Locate and identify every blood parasite.
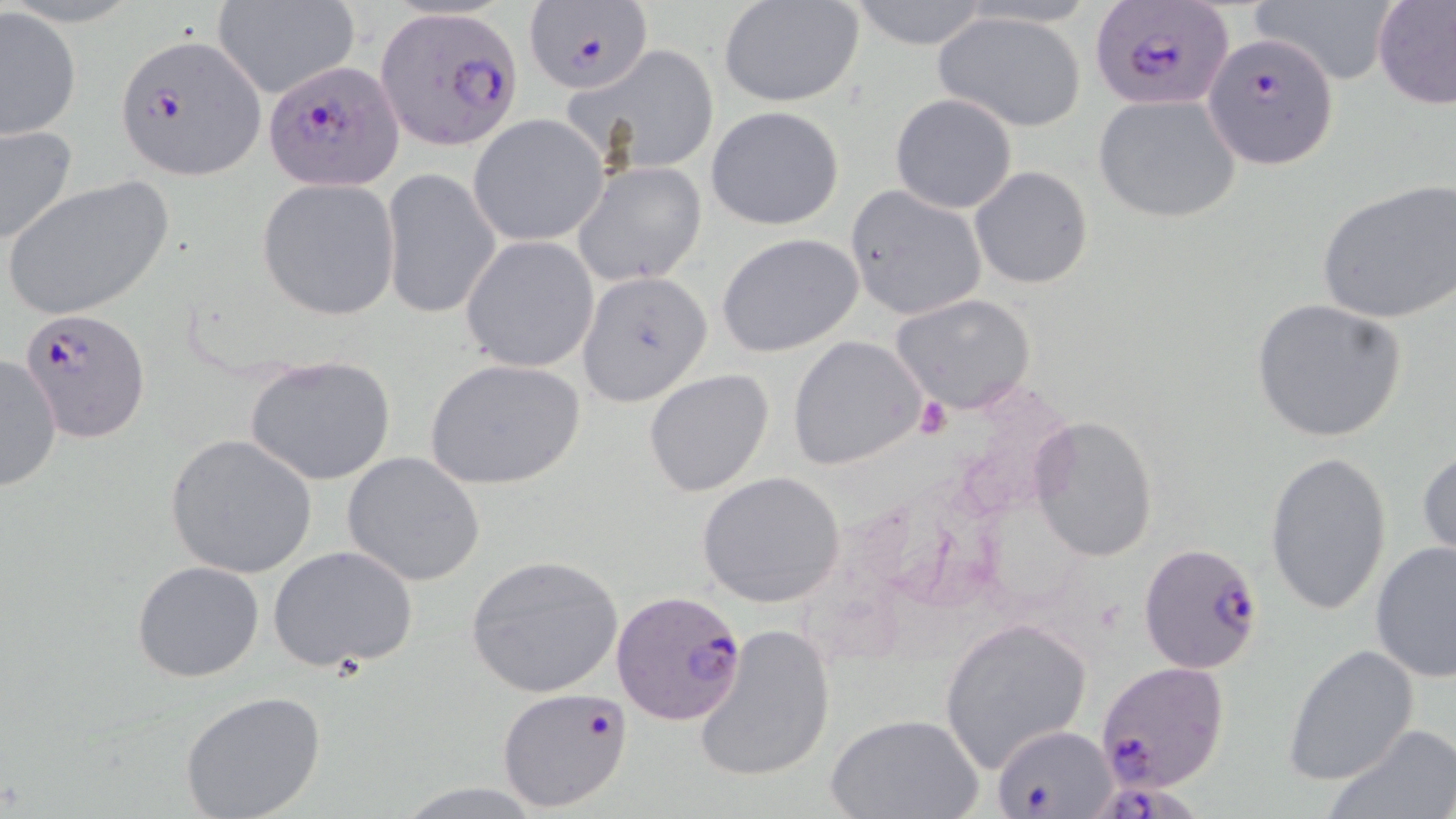
Approximate bounding boxes as named x1/y1/x2/y2 corners in pixels.
Plasmodium falciparum-infected red blood cells: (x1=1090, y1=0, x2=1235, y2=110), (x1=524, y1=4, x2=652, y2=97), (x1=375, y1=7, x2=523, y2=150), (x1=115, y1=32, x2=266, y2=178), (x1=1202, y1=33, x2=1338, y2=171), (x1=263, y1=62, x2=404, y2=192), (x1=19, y1=307, x2=149, y2=440), (x1=1139, y1=540, x2=1266, y2=676), (x1=611, y1=589, x2=749, y2=726), (x1=1096, y1=660, x2=1229, y2=794), (x1=498, y1=688, x2=633, y2=811), (x1=993, y1=725, x2=1115, y2=816), (x1=1094, y1=778, x2=1216, y2=819).
No Plasmodium ovale, Plasmodium malariae, Plasmodium vivax, Babesia divergens, or Trypanosoma brucei observed.

Summary:
  - Platelet locations: (x1=916, y1=396, x2=951, y2=440)
  - Uninfected red blood cell locations: (x1=718, y1=0, x2=864, y2=106), (x1=840, y1=0, x2=999, y2=49), (x1=1247, y1=0, x2=1401, y2=87), (x1=1373, y1=0, x2=1456, y2=109), (x1=212, y1=1, x2=358, y2=102), (x1=0, y1=3, x2=81, y2=141), (x1=933, y1=9, x2=1088, y2=132), (x1=573, y1=46, x2=723, y2=175), (x1=890, y1=93, x2=1018, y2=213), (x1=1095, y1=94, x2=1242, y2=224), (x1=705, y1=105, x2=844, y2=231), (x1=468, y1=114, x2=608, y2=246), (x1=0, y1=123, x2=78, y2=248), (x1=575, y1=162, x2=707, y2=285), (x1=969, y1=166, x2=1092, y2=288), (x1=381, y1=168, x2=501, y2=321), (x1=2, y1=174, x2=174, y2=321), (x1=257, y1=179, x2=401, y2=320), (x1=1317, y1=182, x2=1456, y2=323), (x1=845, y1=184, x2=987, y2=319), (x1=716, y1=233, x2=865, y2=358), (x1=461, y1=236, x2=599, y2=372), (x1=580, y1=268, x2=714, y2=417), (x1=891, y1=294, x2=1034, y2=413), (x1=1248, y1=297, x2=1408, y2=444), (x1=788, y1=335, x2=927, y2=471), (x1=0, y1=353, x2=63, y2=493), (x1=245, y1=355, x2=396, y2=486), (x1=424, y1=359, x2=586, y2=490), (x1=644, y1=369, x2=775, y2=499), (x1=1030, y1=417, x2=1158, y2=561), (x1=166, y1=434, x2=318, y2=579), (x1=1417, y1=447, x2=1456, y2=560), (x1=1264, y1=450, x2=1393, y2=617), (x1=342, y1=452, x2=486, y2=586), (x1=696, y1=471, x2=847, y2=607), (x1=1370, y1=541, x2=1456, y2=685), (x1=267, y1=544, x2=419, y2=673), (x1=465, y1=555, x2=623, y2=697), (x1=133, y1=561, x2=264, y2=682), (x1=937, y1=618, x2=1092, y2=771), (x1=694, y1=622, x2=834, y2=785), (x1=1282, y1=643, x2=1419, y2=786), (x1=179, y1=690, x2=328, y2=818), (x1=826, y1=713, x2=982, y2=819), (x1=1324, y1=723, x2=1456, y2=819), (x1=385, y1=780, x2=556, y2=818)
  - Slide-level diagnosis: Plasmodium falciparum
  - Modality: light microscopy
  - Stain: May-Grünwald-Giemsa
  - Field of view: single
  - Magnification: 1000x
  - Image size: 1456×819 pixels
  - Preparation: thin blood film